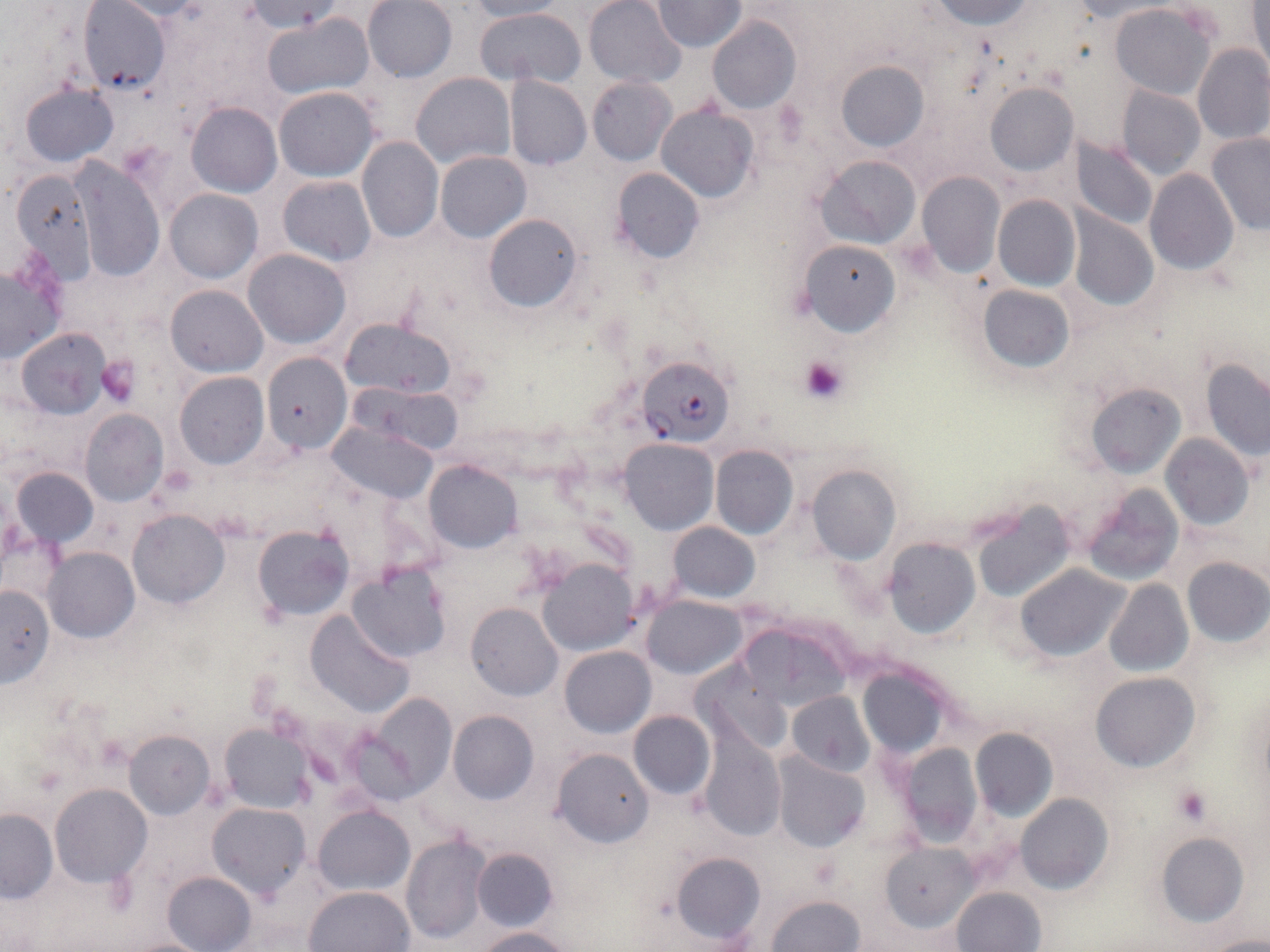 Approximate bounding boxes as named x1/y1/x2/y2 corners in pixels. Platelet locations: (x1=801, y1=354, x2=846, y2=401), (x1=96, y1=355, x2=141, y2=406), (x1=1173, y1=786, x2=1212, y2=826). Uninfected red blood cell locations: (x1=362, y1=0, x2=457, y2=83), (x1=1245, y1=0, x2=1270, y2=73), (x1=77, y1=1, x2=172, y2=95), (x1=107, y1=1, x2=219, y2=21), (x1=468, y1=1, x2=567, y2=21), (x1=583, y1=1, x2=684, y2=87), (x1=652, y1=1, x2=746, y2=51), (x1=930, y1=1, x2=1034, y2=28), (x1=245, y1=2, x2=344, y2=33), (x1=1066, y1=2, x2=1169, y2=22), (x1=1110, y1=4, x2=1214, y2=98), (x1=474, y1=6, x2=585, y2=86), (x1=263, y1=14, x2=372, y2=99), (x1=707, y1=17, x2=801, y2=115), (x1=1192, y1=43, x2=1270, y2=144), (x1=833, y1=59, x2=928, y2=152), (x1=411, y1=72, x2=515, y2=170), (x1=505, y1=76, x2=591, y2=170), (x1=587, y1=77, x2=675, y2=164), (x1=985, y1=83, x2=1077, y2=174), (x1=20, y1=84, x2=118, y2=166), (x1=1117, y1=85, x2=1206, y2=179), (x1=273, y1=86, x2=378, y2=181), (x1=186, y1=102, x2=281, y2=197), (x1=657, y1=103, x2=758, y2=201), (x1=1206, y1=134, x2=1269, y2=234), (x1=357, y1=136, x2=443, y2=243), (x1=1072, y1=136, x2=1157, y2=230), (x1=436, y1=151, x2=530, y2=242), (x1=818, y1=156, x2=920, y2=248), (x1=71, y1=160, x2=164, y2=283), (x1=610, y1=168, x2=703, y2=264), (x1=8, y1=169, x2=95, y2=281), (x1=1145, y1=169, x2=1238, y2=275), (x1=916, y1=173, x2=1005, y2=277), (x1=277, y1=176, x2=376, y2=266), (x1=164, y1=189, x2=262, y2=282), (x1=993, y1=195, x2=1079, y2=290), (x1=1067, y1=209, x2=1158, y2=310), (x1=482, y1=213, x2=582, y2=312), (x1=801, y1=240, x2=901, y2=335), (x1=242, y1=248, x2=350, y2=348), (x1=0, y1=261, x2=65, y2=364), (x1=165, y1=284, x2=267, y2=376), (x1=979, y1=285, x2=1072, y2=371), (x1=343, y1=319, x2=453, y2=400), (x1=17, y1=327, x2=111, y2=418), (x1=262, y1=352, x2=351, y2=454), (x1=1202, y1=357, x2=1270, y2=462), (x1=175, y1=372, x2=268, y2=469), (x1=1084, y1=383, x2=1183, y2=477), (x1=363, y1=385, x2=463, y2=454), (x1=79, y1=410, x2=168, y2=506), (x1=328, y1=421, x2=438, y2=503), (x1=1162, y1=434, x2=1254, y2=530), (x1=620, y1=438, x2=717, y2=535), (x1=711, y1=445, x2=797, y2=538), (x1=424, y1=459, x2=522, y2=553), (x1=807, y1=465, x2=900, y2=563), (x1=12, y1=466, x2=96, y2=548), (x1=1082, y1=485, x2=1185, y2=585), (x1=973, y1=500, x2=1075, y2=602), (x1=128, y1=510, x2=229, y2=608), (x1=668, y1=522, x2=759, y2=601), (x1=253, y1=526, x2=352, y2=620), (x1=884, y1=539, x2=978, y2=638), (x1=44, y1=547, x2=138, y2=642), (x1=1182, y1=557, x2=1270, y2=648), (x1=538, y1=558, x2=639, y2=655), (x1=1014, y1=563, x2=1129, y2=661), (x1=350, y1=564, x2=450, y2=664), (x1=1105, y1=579, x2=1193, y2=676), (x1=0, y1=585, x2=55, y2=690), (x1=643, y1=595, x2=746, y2=679), (x1=466, y1=603, x2=562, y2=701), (x1=304, y1=609, x2=414, y2=718), (x1=741, y1=616, x2=856, y2=714), (x1=560, y1=646, x2=654, y2=738), (x1=855, y1=658, x2=955, y2=761), (x1=696, y1=662, x2=790, y2=757), (x1=1092, y1=673, x2=1200, y2=772), (x1=787, y1=691, x2=874, y2=778), (x1=355, y1=693, x2=459, y2=802), (x1=448, y1=711, x2=539, y2=804), (x1=628, y1=711, x2=714, y2=799), (x1=220, y1=723, x2=316, y2=812), (x1=970, y1=728, x2=1057, y2=819), (x1=698, y1=729, x2=786, y2=838), (x1=125, y1=730, x2=215, y2=818), (x1=894, y1=742, x2=982, y2=845), (x1=552, y1=748, x2=654, y2=847), (x1=771, y1=753, x2=869, y2=852), (x1=51, y1=784, x2=150, y2=885), (x1=1016, y1=794, x2=1112, y2=893), (x1=208, y1=803, x2=311, y2=900), (x1=313, y1=806, x2=413, y2=896), (x1=0, y1=808, x2=57, y2=901), (x1=402, y1=831, x2=491, y2=945), (x1=1154, y1=833, x2=1249, y2=926), (x1=882, y1=843, x2=976, y2=930), (x1=472, y1=848, x2=558, y2=931), (x1=671, y1=852, x2=764, y2=946), (x1=163, y1=872, x2=256, y2=952), (x1=304, y1=886, x2=414, y2=952), (x1=953, y1=887, x2=1045, y2=952), (x1=768, y1=895, x2=863, y2=952), (x1=476, y1=927, x2=573, y2=952), (x1=1206, y1=935, x2=1270, y2=952). Plasmodium falciparum-infected red blood cell locations: (x1=639, y1=355, x2=732, y2=445). Slide-level diagnosis: Plasmodium falciparum. Optical microscopy. Thin blood smear. Image is 1270×952 pixels. May-Grünwald-Giemsa-stained preparation. One field of a larger specimen. 1000x magnification.